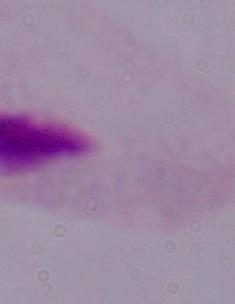
Summary:
  - Modality: micrograph
  - Identification: trichomonad
  - Magnification: 1000x